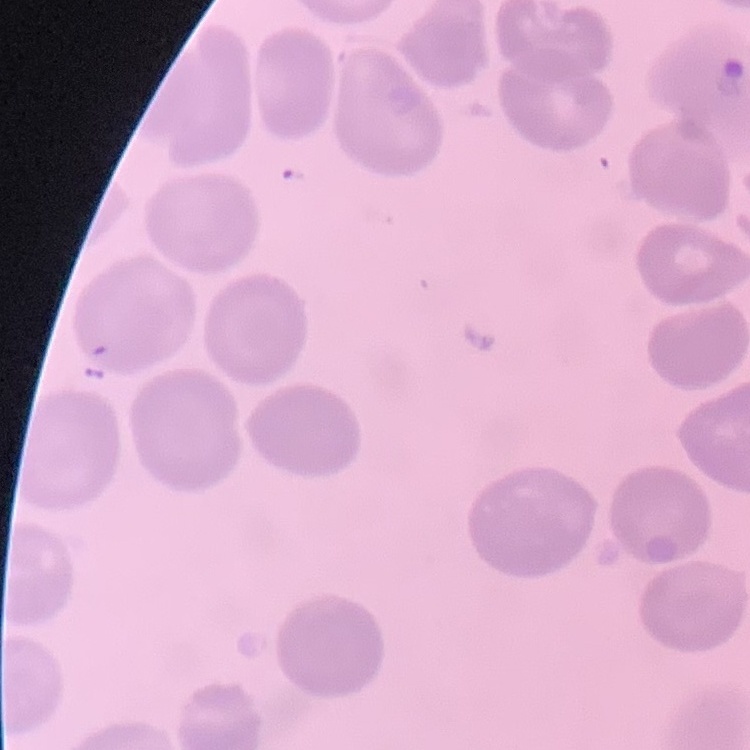

The erythrocytes exhibit no rouleaux formation. One tile cut from a larger photomicrograph. Thin blood smear. Field's or Giemsa stain.